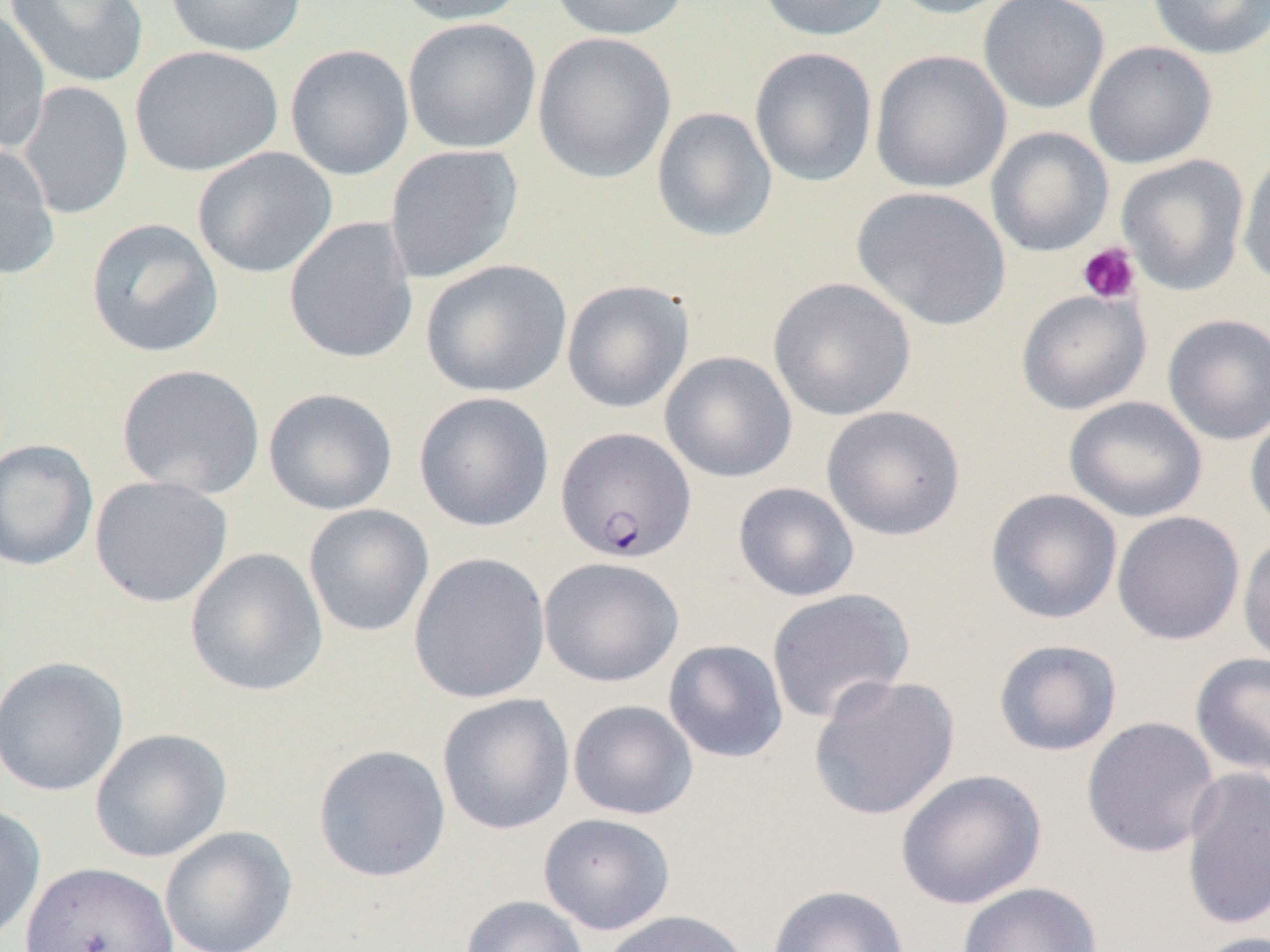

slide-level diagnosis = Plasmodium falciparum
uninfected red blood cell locations (subset) = approximate bounding boxes as [x1, y1, x2, y2] in pixels: [165, 0, 308, 57], [388, 0, 530, 25], [547, 0, 692, 40], [756, 0, 892, 42], [883, 0, 1022, 19], [978, 0, 1110, 115], [1146, 0, 1270, 60], [6, 1, 150, 89], [0, 9, 51, 156], [403, 17, 541, 154], [533, 32, 677, 184], [1083, 40, 1217, 169], [129, 44, 284, 177], [285, 44, 415, 181], [749, 47, 878, 187], [870, 50, 1011, 194], [17, 81, 134, 220], [651, 106, 778, 242], [0, 141, 60, 280], [383, 145, 523, 284], [193, 146, 337, 279], [1237, 147, 1270, 289], [1116, 155, 1249, 295], [851, 186, 1012, 331], [85, 217, 224, 358], [284, 217, 419, 364], [420, 259, 573, 398], [768, 277, 916, 421], [561, 279, 694, 413], [1015, 290, 1151, 414], [1162, 313, 1270, 446], [660, 351, 797, 483], [116, 363, 266, 499], [263, 387, 398, 515], [413, 391, 555, 532], [1064, 396, 1207, 523], [821, 405, 966, 540], [1245, 409, 1270, 535], [0, 438, 99, 571], [89, 475, 233, 608], [733, 482, 860, 602], [985, 488, 1123, 625], [303, 504, 435, 637], [1111, 511, 1246, 645], [1237, 533, 1270, 668], [184, 547, 329, 697], [408, 552, 551, 704], [538, 557, 684, 688], [766, 587, 916, 725], [663, 639, 789, 763], [992, 639, 1123, 757], [1190, 652, 1270, 779], [0, 655, 130, 797], [808, 674, 961, 821], [437, 693, 575, 835], [568, 700, 699, 820], [1080, 716, 1222, 859], [90, 728, 233, 863], [313, 744, 451, 883], [1179, 766, 1270, 931], [896, 768, 1047, 909], [0, 802, 46, 944], [538, 813, 676, 935], [160, 826, 297, 952], [20, 861, 179, 952], [956, 881, 1102, 952], [766, 884, 909, 952], [460, 894, 589, 952], [597, 909, 755, 952], [1188, 930, 1269, 952]
platelet locations (subset) = approximate bounding boxes as [x1, y1, x2, y2] in pixels: [1077, 241, 1142, 305]
image size = 1270×952 pixels
magnification = 1000x
preparation = thin blood smear
Plasmodium falciparum-infected red blood cell locations = approximate bounding boxes as [x1, y1, x2, y2] in pixels: [555, 427, 697, 564]
field of view = one of a larger specimen
modality = light microscopy